Assess this cell for malaria.
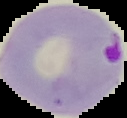
Parasitized.

image type = cell region segmented out of the field of view; surrounding area masked to black
preparation = thin blood film
image size = 127×118 pixels